Report the malaria status of this cell.
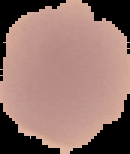
Uninfected.

Cell region segmented out of the field of view; the surrounding area is masked to black. From a thin blood smear. Image is 130×154 pixels.